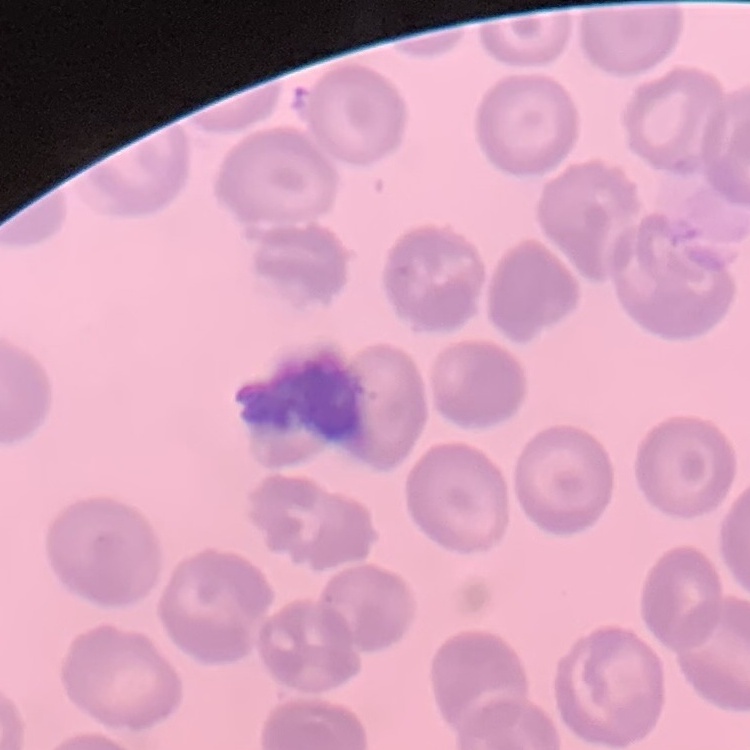
erythrocyte morphology = no rouleaux formation
image type = square crop of a larger photomicrograph
stain = Field's or Giemsa
preparation = thin blood film